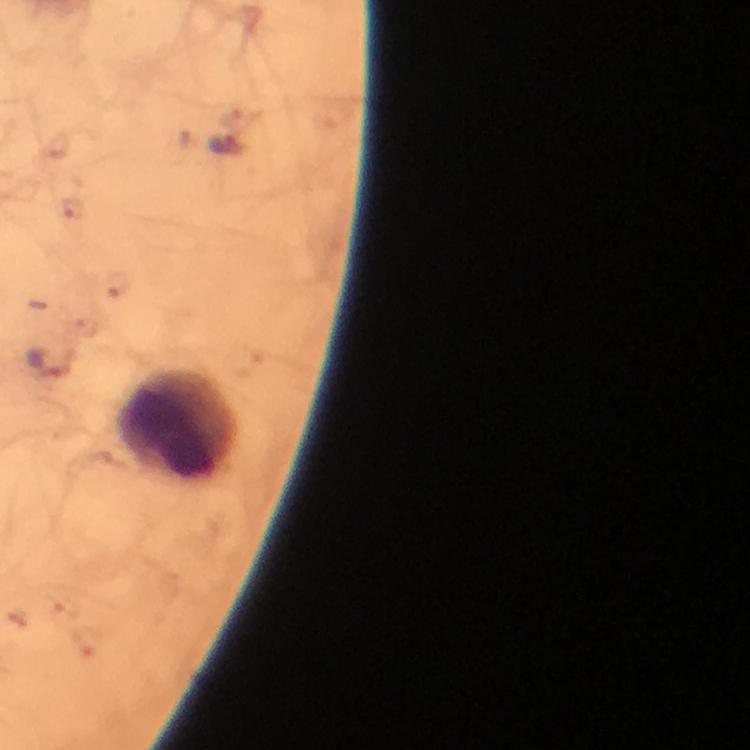

Approximate centers as (x, y) in pixels. Plasmodium parasite locations: (226, 148), (53, 356). Leukocyte locations: (180, 426). Thick blood film. From a malaria diagnostic workup. Smartphone photograph taken through a microscope. A crop from one field of view. Image is 750×750 pixels. At 100x magnification. Giemsa-stained preparation. Immersion oil applied.